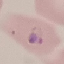
result = malaria parasites identified
image type = automatically extracted cell patch, resized to 64 × 64 pixels
preparation = thin smear
capture = smartphone through the microscope eyepiece
stain = Giemsa